Identify the blood parasite species.
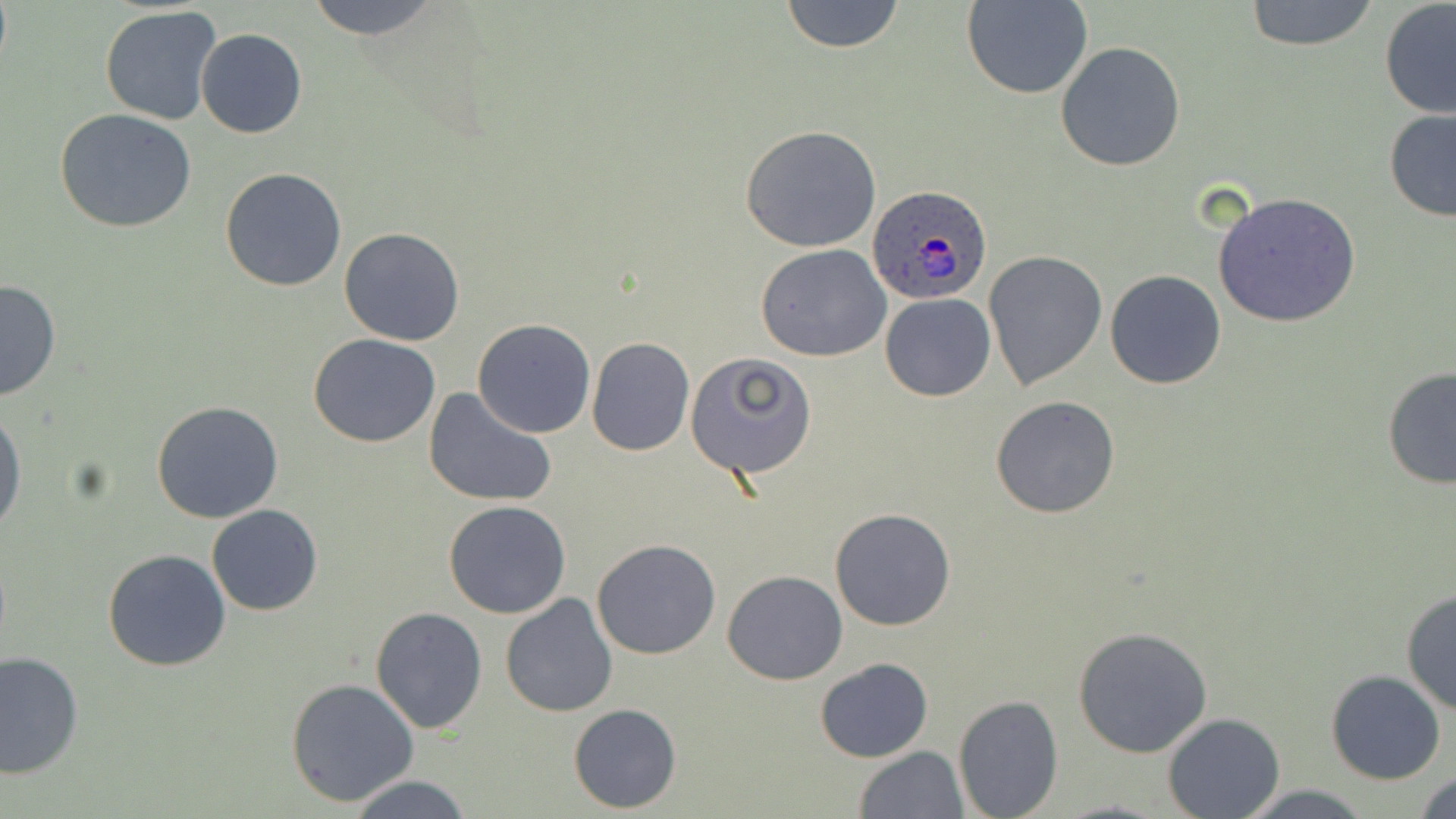
Plasmodium ovale.

Approximate bounding boxes as (x1,y1)-(x2,y2) corner pairs in pixels. Plasmodium ovale-infected red blood cell locations: (867,187)-(992,305). Uninfected red blood cell locations: (303,0)-(442,42), (779,0)-(906,54), (964,0)-(1093,100), (1242,0)-(1379,51), (1379,2)-(1456,120), (100,6)-(222,126), (195,29)-(308,139), (1055,40)-(1186,172), (55,108)-(196,233), (1383,108)-(1456,223), (740,125)-(882,252), (220,168)-(348,292), (1212,191)-(1361,327), (339,227)-(467,346), (755,243)-(892,361), (985,252)-(1108,388), (1104,270)-(1227,390), (0,279)-(62,402), (880,292)-(996,402), (472,319)-(596,438), (308,334)-(440,447), (587,337)-(695,455), (687,353)-(814,477), (1381,366)-(1456,490), (423,385)-(556,507), (990,394)-(1121,519), (150,399)-(284,523), (0,408)-(25,536), (443,499)-(572,619), (206,504)-(324,616), (830,507)-(957,632), (591,538)-(722,659), (101,548)-(231,671), (722,570)-(848,685), (1401,588)-(1456,717), (501,593)-(617,717), (370,607)-(488,733), (1073,626)-(1213,759), (1,651)-(83,778), (814,658)-(934,763), (1325,671)-(1446,785), (285,678)-(419,807), (953,694)-(1063,818), (569,703)-(681,812), (1162,713)-(1286,819), (852,746)-(969,819), (1414,768)-(1456,819), (347,774)-(474,818), (1233,783)-(1376,819). Light microscopy. Image is 1456×819 pixels. One field of a larger specimen. May-Grünwald-Giemsa stain. Thin blood smear. 1000x magnification.